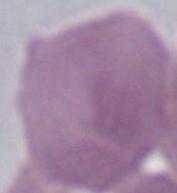

{
  "modality": "micrograph",
  "magnification": "1000x",
  "identification": "erythrocyte"
}